Locate every Plasmodium ovale-infected red blood cell.
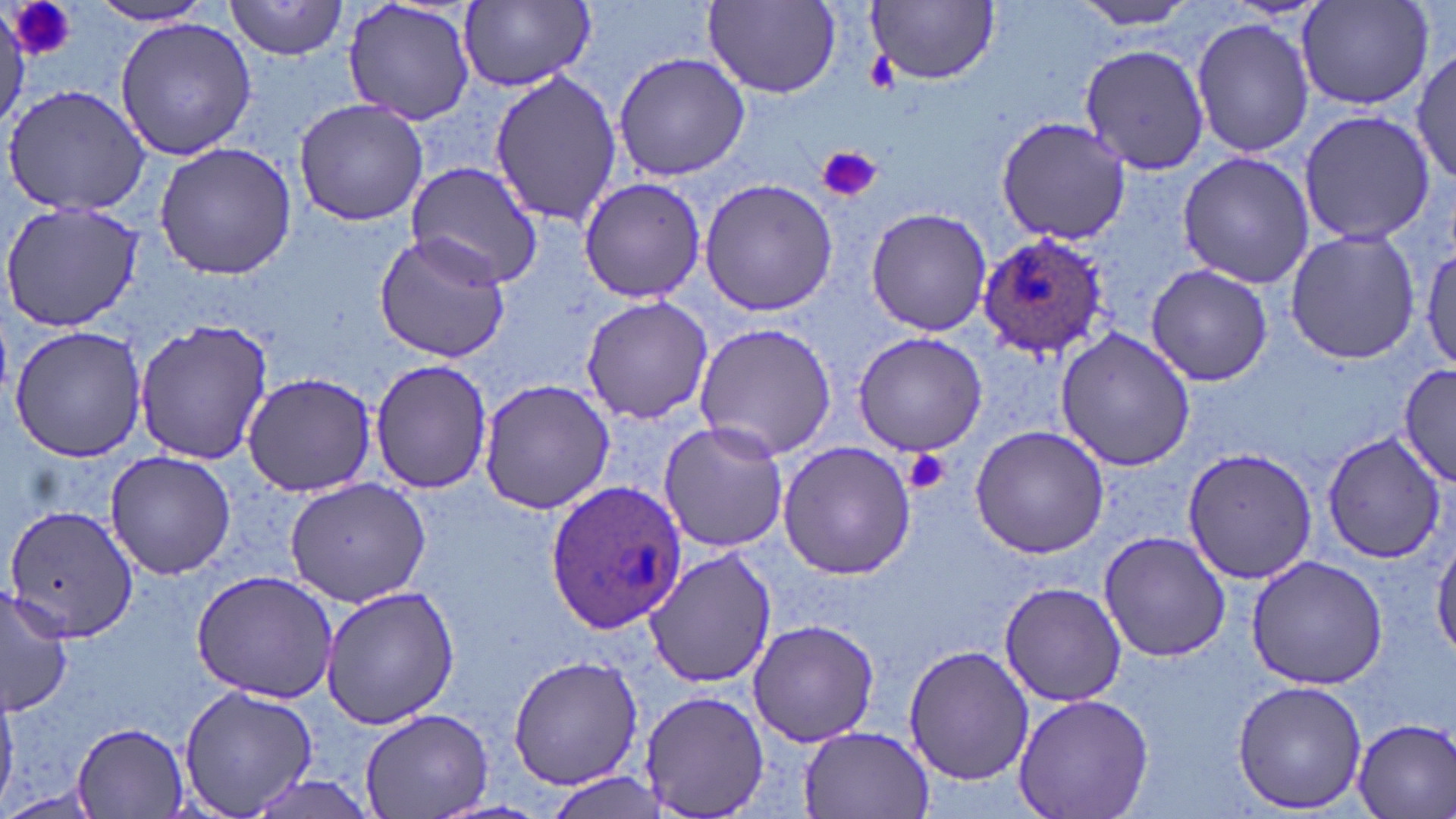
Approximate bounding boxes as (x1, y1, x2, y2) in pixels.
Plasmodium ovale-infected red blood cells: (977, 233, 1107, 358), (546, 478, 687, 640).

slide-level diagnosis = Plasmodium ovale
stain = May-Grünwald-Giemsa
magnification = 1000x
field of view = single
uninfected red blood cell locations = approximate bounding boxes as (x1, y1, x2, y2) in pixels: (225, 0, 348, 60), (341, 0, 479, 128), (1073, 0, 1210, 30), (89, 1, 217, 27), (460, 1, 595, 89), (870, 1, 999, 85), (1298, 1, 1434, 112), (704, 2, 840, 98), (113, 16, 260, 161), (1191, 16, 1313, 160), (1079, 42, 1211, 176), (1412, 49, 1456, 186), (612, 52, 749, 182), (487, 68, 624, 227), (4, 86, 153, 216), (294, 98, 428, 227), (1298, 107, 1435, 248), (995, 116, 1132, 244), (154, 143, 298, 282), (1175, 149, 1317, 290), (406, 162, 542, 288), (577, 176, 708, 302), (699, 178, 839, 317), (1, 200, 144, 334), (865, 206, 992, 337), (1284, 228, 1423, 366), (373, 233, 514, 364), (1419, 242, 1454, 377), (1146, 264, 1274, 387), (580, 295, 712, 425), (132, 317, 273, 467), (693, 321, 838, 462), (9, 325, 148, 464), (1054, 328, 1199, 472), (851, 332, 990, 458), (369, 357, 492, 495), (1398, 361, 1454, 487), (244, 371, 377, 496), (477, 379, 614, 515), (658, 421, 788, 555), (969, 424, 1109, 559), (1320, 430, 1447, 565), (776, 440, 918, 580), (1180, 445, 1320, 583), (103, 450, 237, 579), (283, 477, 431, 608), (3, 503, 140, 645), (1098, 530, 1231, 662), (1432, 536, 1456, 663), (645, 547, 778, 688), (1245, 553, 1392, 691), (191, 568, 339, 703), (998, 579, 1129, 707), (321, 585, 462, 730), (0, 586, 74, 717), (745, 619, 880, 748), (903, 644, 1034, 786), (508, 654, 643, 790), (1231, 680, 1368, 814), (177, 681, 318, 819), (637, 689, 770, 817), (1013, 692, 1153, 819), (359, 707, 493, 819), (1350, 716, 1456, 819), (70, 721, 192, 816), (798, 726, 934, 819), (547, 772, 667, 817), (0, 785, 106, 819)
modality = light microscopy
preparation = thin blood film
platelet locations = approximate bounding boxes as (x1, y1, x2, y2) in pixels: (8, 1, 75, 61), (819, 147, 881, 203), (905, 449, 949, 495)
image size = 1456×819 pixels